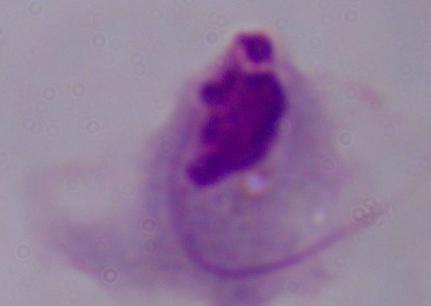

Summary:
  - Identification: trichomonad
  - Magnification: 1000x
  - Modality: photomicrograph